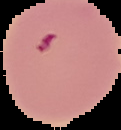 From a thin blood film. Image is 121×130 pixels. Cell region segmented out of the field of view; the surrounding area is masked to black. Malaria status: parasitized.